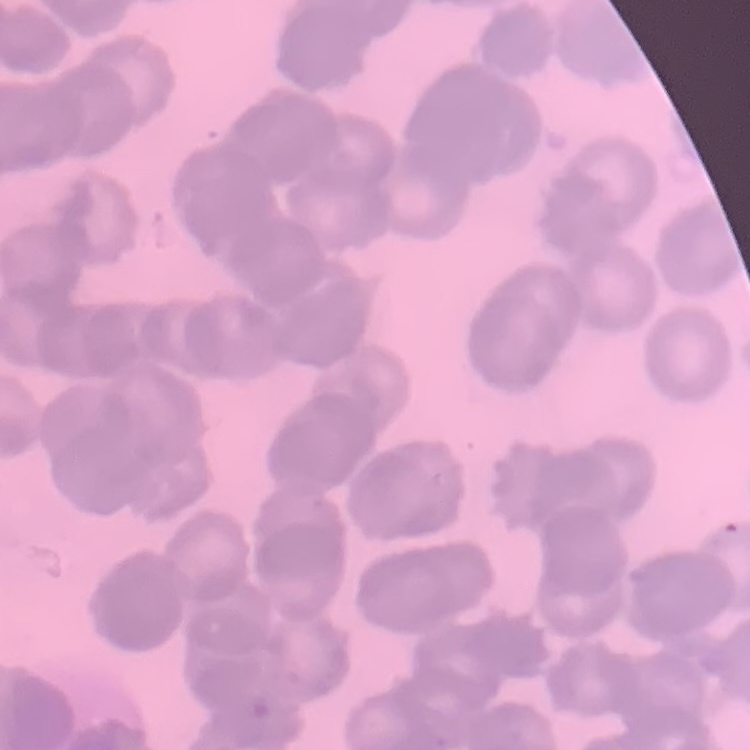

The erythrocytes show rouleaux formation. Square crop of a larger photomicrograph. Field's or Giemsa stain. Thin peripheral smear.